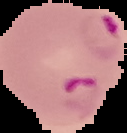

malaria status = parasitized
preparation = thin blood film
image type = segmented cell region with the area outside set to black
image size = 127×133 pixels